Assess the morphology of the red blood cells.
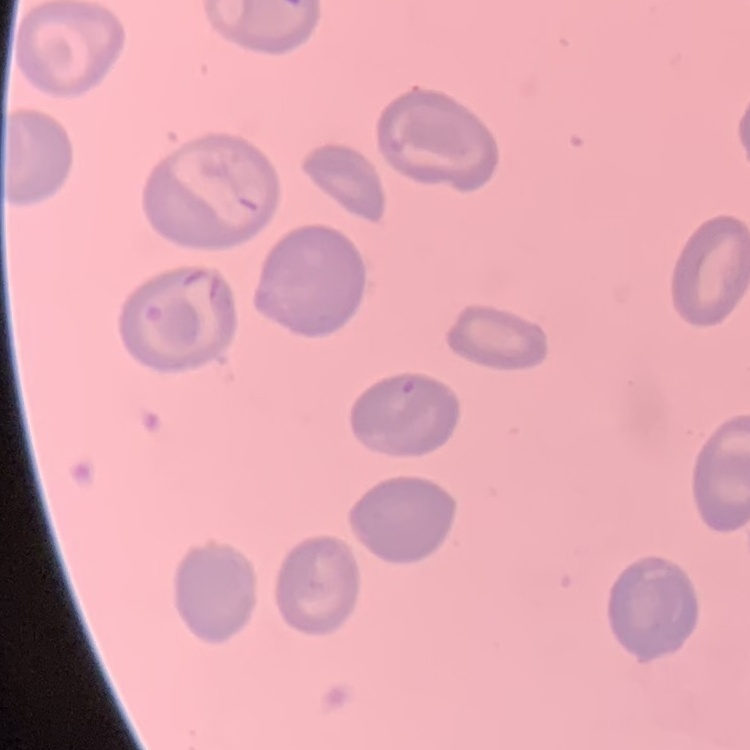

No rouleaux formation.

preparation = thin peripheral smear
image type = square crop of a larger photomicrograph
stain = Field's or Giemsa